Describe the morphology of the red blood cells.
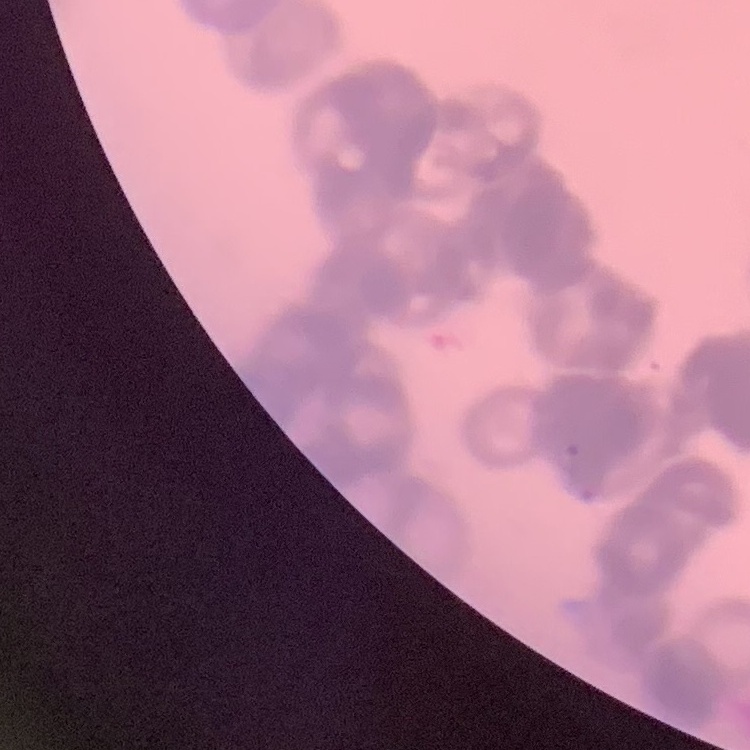
Rouleaux formation.

Thin peripheral smear. One tile cut from a larger photomicrograph. Stained with either Field's or Giemsa.